Locate every Plasmodium ovale-infected red blood cell.
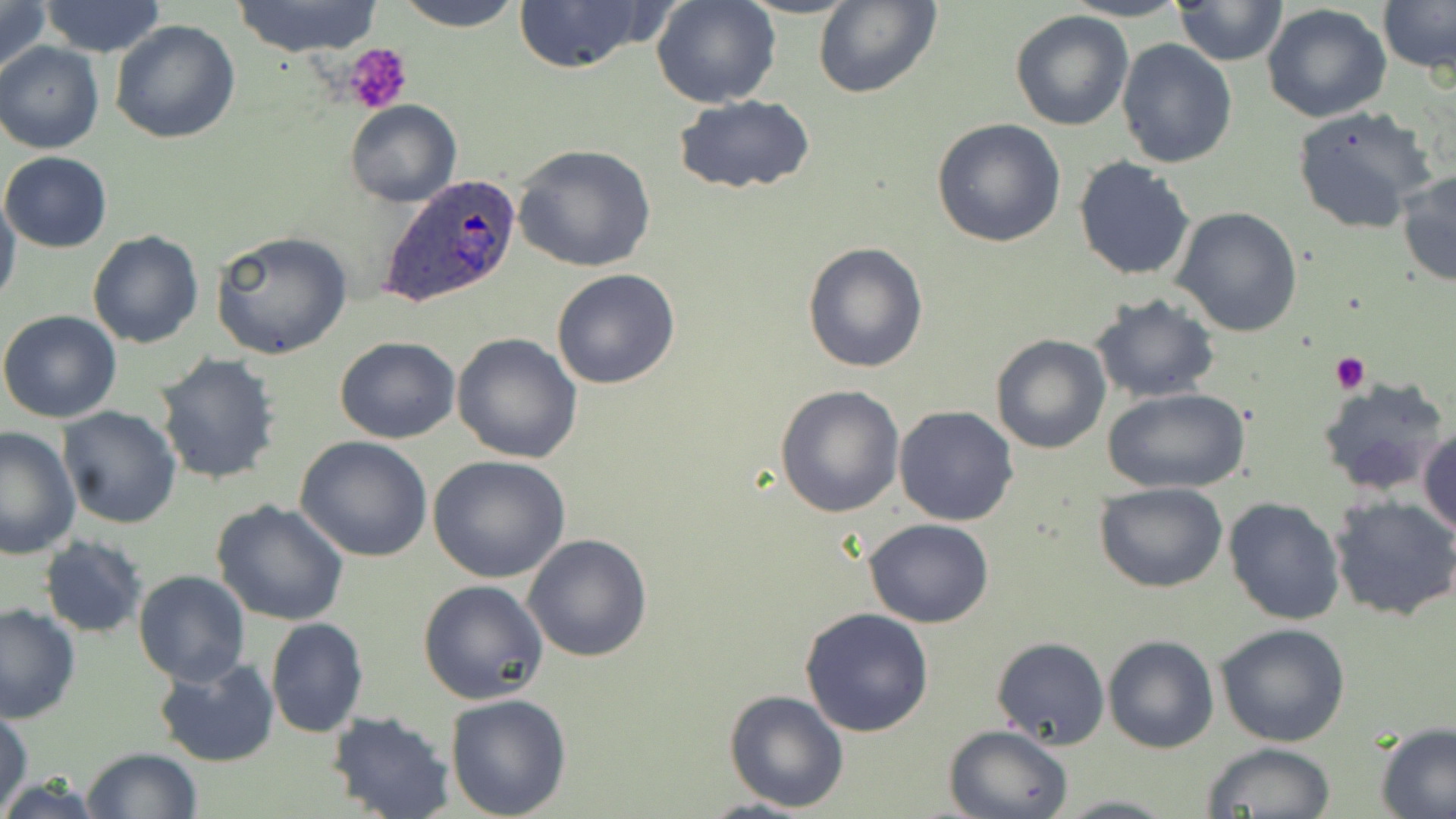
Approximate bounding boxes as named x1/y1/x2/y2 corners in pixels.
Plasmodium ovale-infected red blood cells: (x1=379, y1=173, x2=523, y2=309).

Uninfected red blood cell locations: (x1=0, y1=0, x2=51, y2=84), (x1=37, y1=0, x2=169, y2=57), (x1=231, y1=0, x2=385, y2=56), (x1=387, y1=0, x2=529, y2=30), (x1=650, y1=0, x2=782, y2=108), (x1=813, y1=0, x2=943, y2=100), (x1=1061, y1=0, x2=1191, y2=22), (x1=1379, y1=0, x2=1455, y2=74), (x1=509, y1=1, x2=656, y2=74), (x1=1172, y1=1, x2=1287, y2=64), (x1=1262, y1=2, x2=1393, y2=124), (x1=1009, y1=10, x2=1134, y2=131), (x1=109, y1=19, x2=241, y2=144), (x1=0, y1=40, x2=104, y2=154), (x1=1116, y1=40, x2=1238, y2=170), (x1=673, y1=95, x2=817, y2=196), (x1=344, y1=100, x2=462, y2=207), (x1=1291, y1=106, x2=1437, y2=237), (x1=932, y1=118, x2=1066, y2=248), (x1=511, y1=143, x2=658, y2=272), (x1=1, y1=150, x2=111, y2=251), (x1=1073, y1=156, x2=1196, y2=281), (x1=1397, y1=168, x2=1456, y2=287), (x1=0, y1=190, x2=21, y2=308), (x1=1171, y1=206, x2=1303, y2=337), (x1=87, y1=230, x2=203, y2=349), (x1=209, y1=230, x2=353, y2=360), (x1=801, y1=243, x2=928, y2=373), (x1=550, y1=269, x2=680, y2=390), (x1=1089, y1=293, x2=1222, y2=403), (x1=0, y1=309, x2=122, y2=423), (x1=451, y1=333, x2=584, y2=464), (x1=989, y1=334, x2=1112, y2=454), (x1=334, y1=336, x2=461, y2=443), (x1=153, y1=352, x2=282, y2=486), (x1=1317, y1=377, x2=1449, y2=499), (x1=774, y1=384, x2=906, y2=518), (x1=1105, y1=387, x2=1249, y2=495), (x1=894, y1=406, x2=1019, y2=527), (x1=57, y1=407, x2=183, y2=530), (x1=0, y1=426, x2=81, y2=560), (x1=1418, y1=426, x2=1456, y2=540), (x1=294, y1=436, x2=433, y2=562), (x1=427, y1=454, x2=570, y2=582), (x1=1095, y1=481, x2=1228, y2=593), (x1=1223, y1=496, x2=1345, y2=625), (x1=1329, y1=496, x2=1456, y2=622), (x1=212, y1=499, x2=349, y2=626), (x1=864, y1=518, x2=994, y2=629), (x1=522, y1=533, x2=655, y2=663), (x1=39, y1=537, x2=147, y2=638), (x1=132, y1=570, x2=251, y2=687), (x1=418, y1=579, x2=548, y2=704), (x1=0, y1=603, x2=80, y2=724), (x1=799, y1=607, x2=935, y2=737), (x1=265, y1=618, x2=368, y2=737), (x1=1215, y1=624, x2=1352, y2=748), (x1=1102, y1=634, x2=1218, y2=754), (x1=991, y1=636, x2=1109, y2=752), (x1=152, y1=657, x2=279, y2=768), (x1=724, y1=688, x2=851, y2=812), (x1=444, y1=693, x2=572, y2=818), (x1=0, y1=705, x2=34, y2=814), (x1=325, y1=710, x2=455, y2=819), (x1=943, y1=723, x2=1072, y2=818), (x1=1373, y1=723, x2=1456, y2=818), (x1=1200, y1=743, x2=1337, y2=818), (x1=81, y1=747, x2=202, y2=819), (x1=1053, y1=794, x2=1180, y2=818). Platelet locations: (x1=343, y1=45, x2=411, y2=115), (x1=1331, y1=352, x2=1370, y2=394). Slide-level diagnosis: Plasmodium ovale. May-Grünwald-Giemsa stain. Optical microscopy. Image is 1456×819 pixels. 1000x magnification. One field of a larger specimen. Thin blood smear.